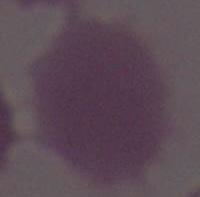

A red blood cell is shown. Captured at 1000x magnification. Photomicrograph.